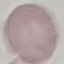
Summary:
  - Malaria status: uninfected
  - Stain: Giemsa
  - Image type: cell patch, automatically extracted from a larger field of view and resized to 64 × 64 pixels
  - Capture: smartphone through the microscope eyepiece
  - Preparation: thin smear